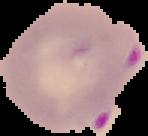

result = Plasmodium parasites detected
preparation = thin blood smear
image type = cell region segmented out of the field of view; surrounding area masked to black
image size = 148×136 pixels